Describe the morphology of the red blood cells.
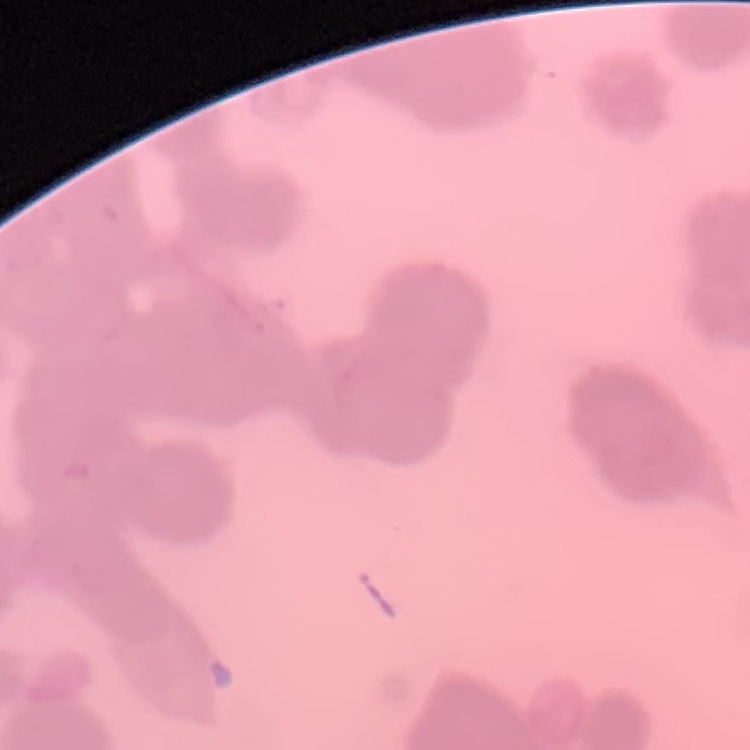
Rouleaux formation.

stain: Field's or Giemsa
image_type: square crop of a larger photomicrograph
preparation: thin blood smear